Assess the morphology of the erythrocytes.
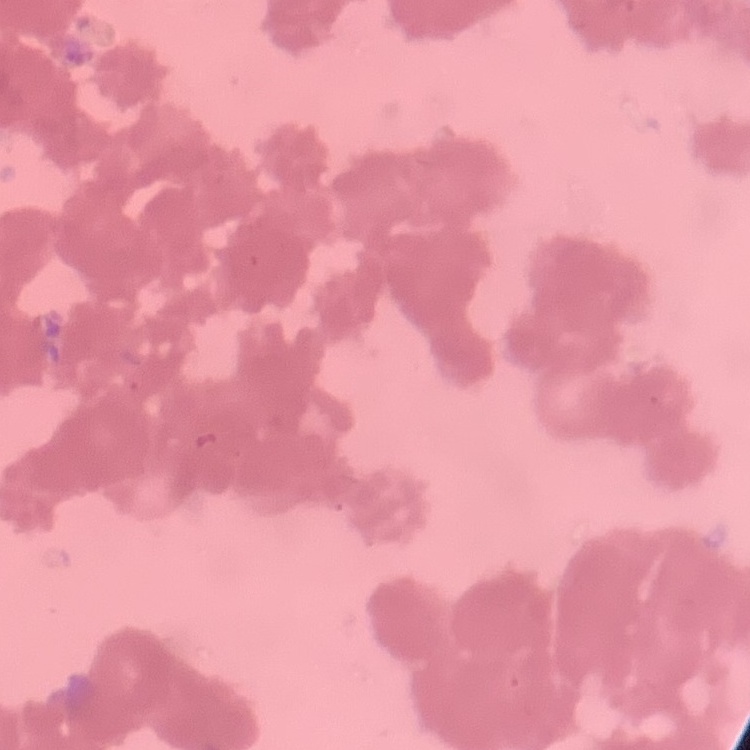

They show rouleaux formation.

image type = one tile cut from a larger photomicrograph
stain = Field's or Giemsa
preparation = thin blood smear